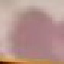
malaria status = uninfected
stain = Giemsa
preparation = thin blood smear
capture = smartphone camera at the microscope eyepiece
image type = cell patch, automatically extracted from a larger field of view and resized to 64 × 64 pixels